Report the malaria status of this cell.
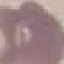
Uninfected.

{
  "stain": "Giemsa",
  "image_type": "cell patch, automatically extracted from a larger field of view and resized to 64 × 64 pixels",
  "capture": "smartphone camera at the microscope eyepiece",
  "preparation": "thin blood film"
}